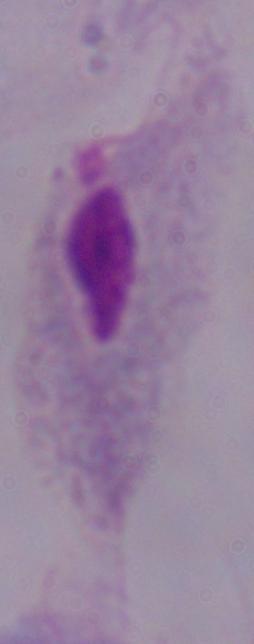
A trichomonad is seen. Micrograph. Captured at 1000x magnification.